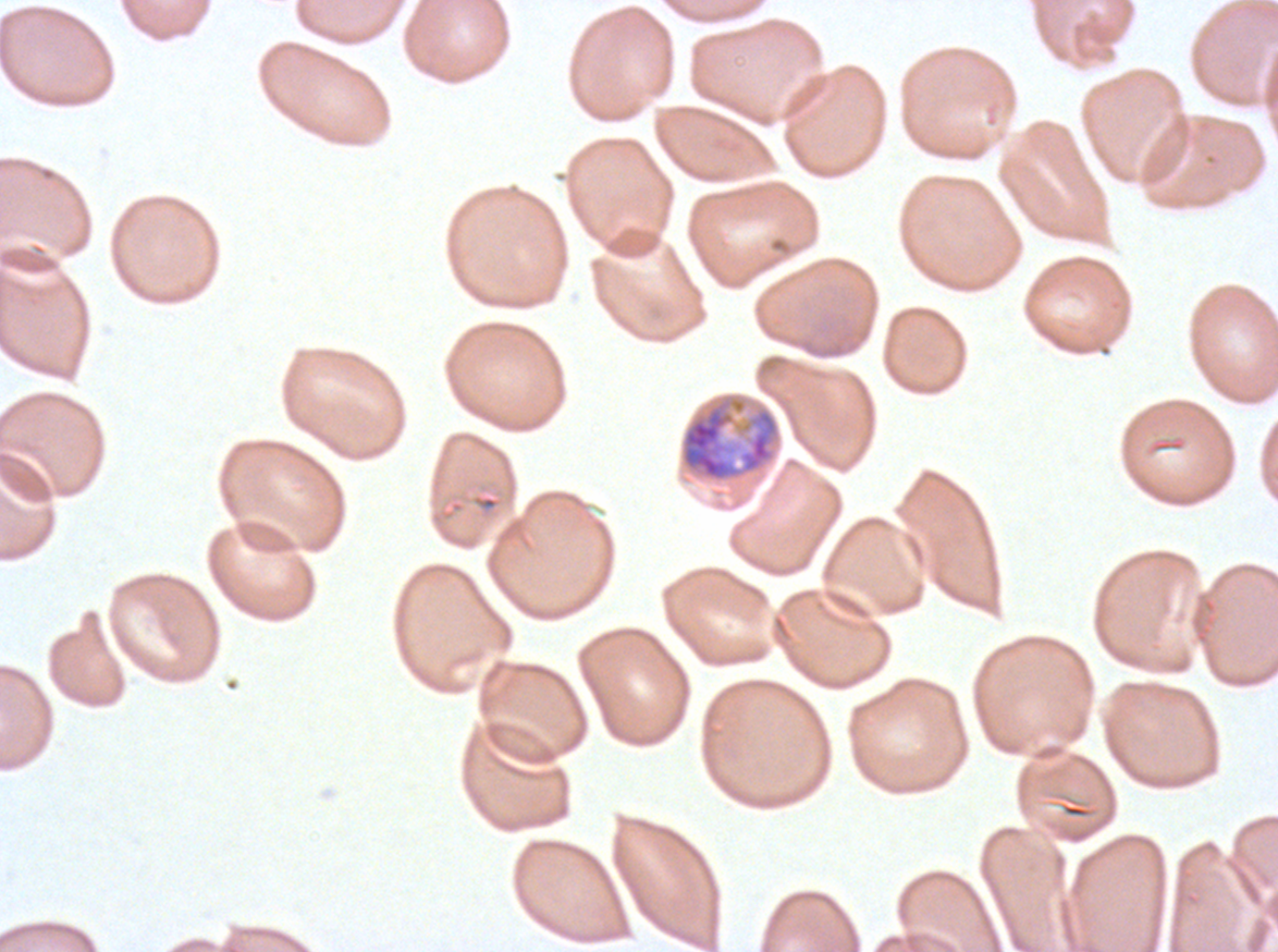
Approximate bounding boxes as [x1, y1, x2, y2] in pixels.
Summary:
  - Late trophozoite locations: [678, 391, 782, 484]
  - Preparation: thin blood film
  - Stain: Giemsa
  - Specimen: Plasmodium falciparum cultured ex vivo for 24 to 48 hours, from a patient in The Gambia
  - Image size: 1278×952 pixels
  - Field of view: sub-image separated from a larger composite